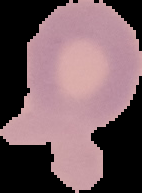 Image is 142×193 pixels. Segmented cell region on a black background. From a thin blood smear. Malaria status: uninfected.